Give the position of each Plasmodium falciparum parasite with its life-cycle stage, each leukocyte, and any debris.
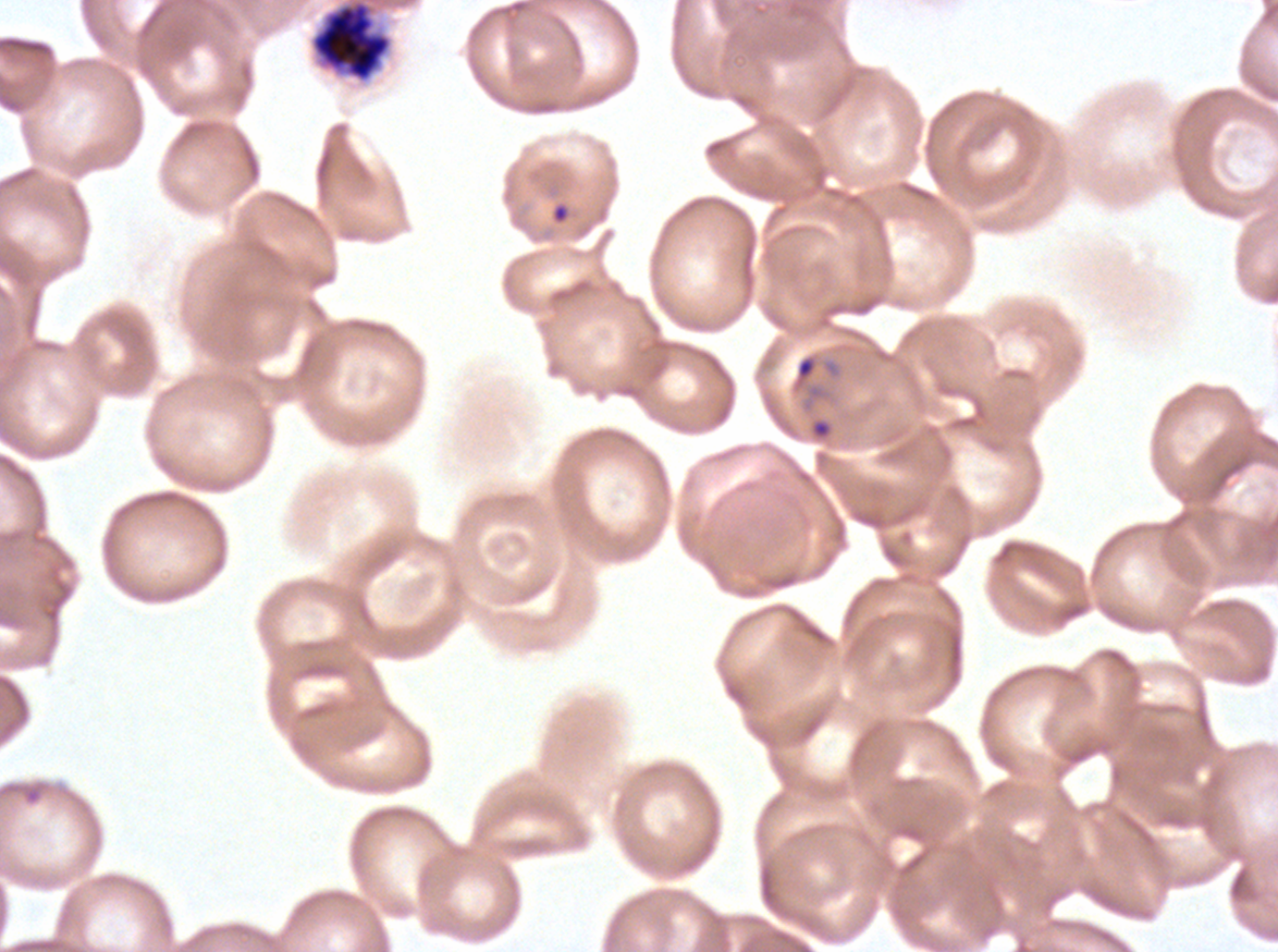

Approximate bounding boxes as {x1, y1, x2, y2} in pixels.
Rings: {553, 204, 568, 222}, {792, 353, 819, 390}, {0, 780, 48, 806}.
Late schizonts: {310, 0, 392, 82}.
No late-ring/early-trophozoite forms, mid trophozoites, late trophozoites, early schizonts, segmenters, gametocytes, leukocytes, or debris observed.

image size = 1278×952 pixels
life-cycle stages observed = ring, late schizont
field of view = one sub-image of a larger composite
specimen = Plasmodium falciparum from a patient in The Gambia, cultured ex vivo for 24 to 48 hours
stain = Giemsa
preparation = thin blood smear